Describe the morphology of the erythrocytes.
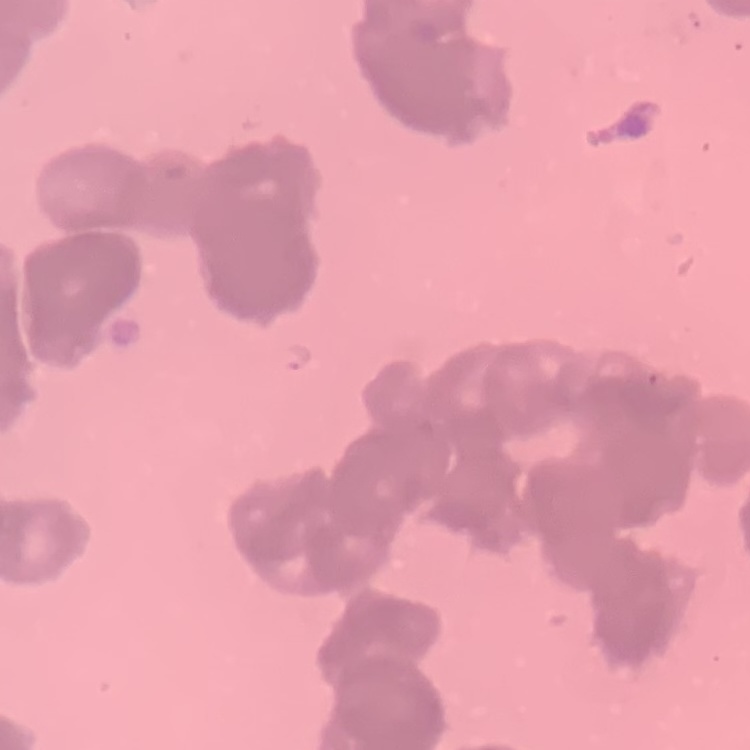
Rouleaux formation.

Summary:
  - Image type: one tile cut from a larger photomicrograph
  - Preparation: thin blood film
  - Stain: Field's or Giemsa